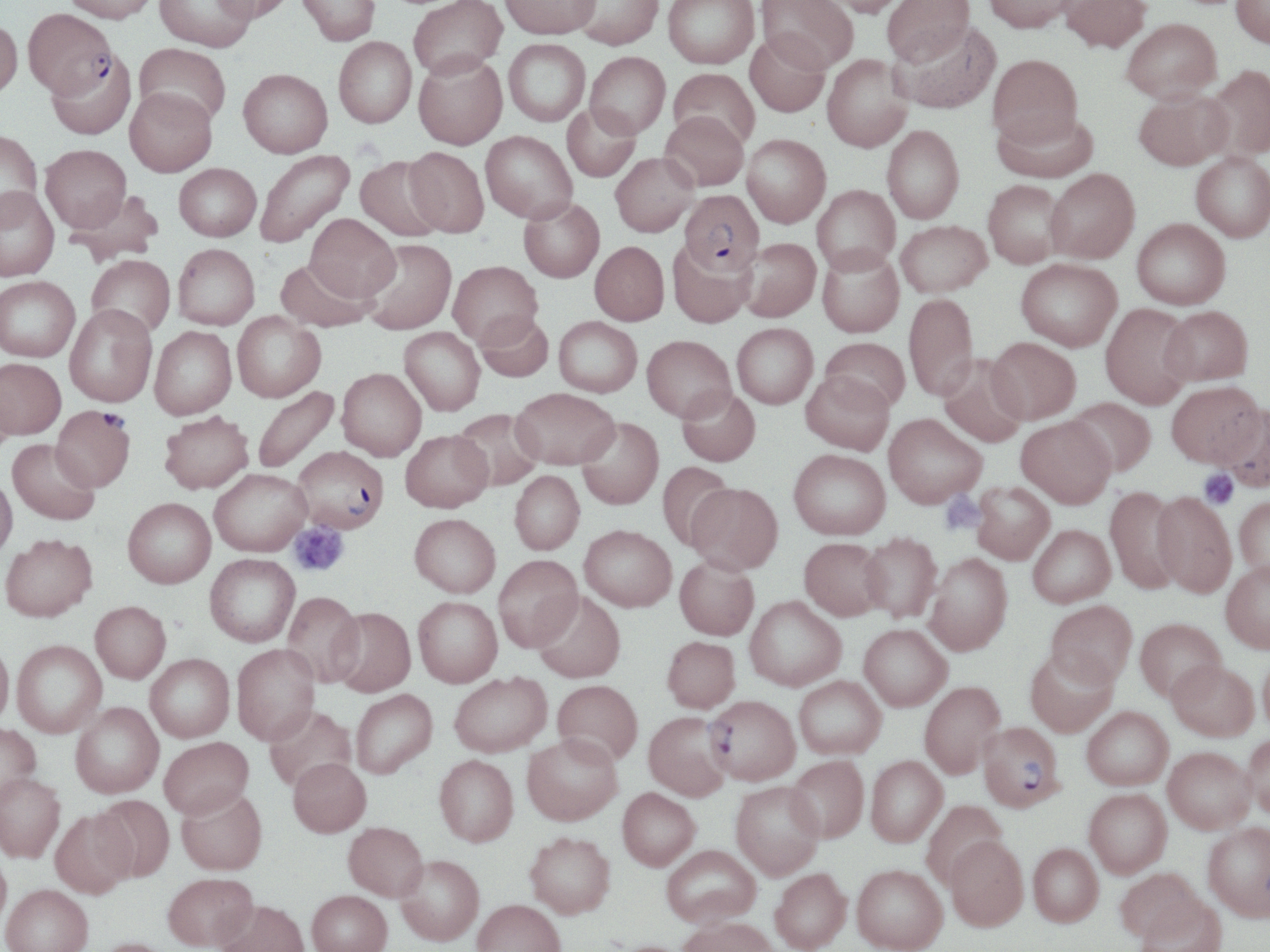
Approximate bounding boxes as (x1,y1)-(x2,y2) corner pairs in pixels. Plasmodium falciparum-infected red blood cell locations: (24,9)-(115,102), (679,190)-(764,275), (51,406)-(135,492), (293,445)-(389,533), (705,695)-(800,785), (978,721)-(1064,811). Uninfected red blood cell locations: (62,0)-(158,26), (154,0)-(258,53), (210,0)-(294,26), (296,0)-(380,46), (409,0)-(507,82), (500,0)-(600,39), (570,0)-(664,51), (663,0)-(759,70), (756,0)-(857,73), (820,0)-(908,18), (883,0)-(975,68), (984,0)-(1079,34), (1059,0)-(1151,55), (1232,0)-(1270,49), (0,19)-(23,102), (1121,20)-(1221,105), (892,21)-(1001,114), (745,33)-(831,118), (333,38)-(417,130), (503,39)-(590,127), (134,44)-(230,128), (585,52)-(670,139), (47,53)-(136,141), (822,54)-(913,152), (988,54)-(1084,148), (413,55)-(507,151), (1205,65)-(1270,161), (668,68)-(759,151), (238,70)-(332,160), (125,90)-(217,178), (1134,90)-(1233,170), (562,104)-(641,182), (993,108)-(1098,183), (660,111)-(749,191), (882,125)-(964,223), (481,130)-(577,223), (0,131)-(43,224), (742,134)-(831,227), (40,146)-(131,233), (404,147)-(489,238), (255,150)-(354,249), (611,152)-(700,237), (1191,152)-(1270,242), (355,156)-(446,243), (174,163)-(262,242), (1045,168)-(1139,263), (983,179)-(1067,268), (812,185)-(900,274), (0,188)-(59,282), (66,189)-(163,267), (518,198)-(605,282), (305,214)-(400,301), (1132,218)-(1231,309), (896,220)-(992,297), (736,237)-(821,322), (358,238)-(457,335), (667,239)-(756,327), (590,241)-(669,325), (173,243)-(260,330), (817,246)-(904,338), (87,255)-(175,339), (275,257)-(377,332), (1016,258)-(1122,350), (448,260)-(542,348), (0,276)-(80,362), (903,293)-(978,399), (1100,303)-(1195,408), (64,305)-(157,407), (1161,305)-(1253,385), (474,310)-(554,382), (232,312)-(326,402), (554,316)-(642,397), (732,323)-(818,408), (149,326)-(237,419), (398,327)-(485,415), (642,335)-(735,422), (987,336)-(1080,423), (819,337)-(910,413), (938,354)-(1028,448), (0,357)-(66,439), (337,368)-(427,461), (800,370)-(894,455), (1,379)-(16,464), (1167,380)-(1265,467), (252,385)-(340,474), (677,386)-(761,466), (511,387)-(620,469), (1066,397)-(1156,476), (1221,402)-(1270,492), (452,407)-(545,491), (159,410)-(254,494), (883,413)-(986,508), (1016,416)-(1116,507), (576,417)-(664,509), (400,429)-(493,512), (8,439)-(100,525), (788,448)-(890,539), (657,461)-(736,550), (209,468)-(310,556), (510,470)-(584,555), (0,474)-(17,560), (972,481)-(1055,564), (686,482)-(783,575), (1105,486)-(1185,593), (1151,492)-(1236,596), (1235,495)-(1270,582), (123,498)-(216,588), (409,513)-(501,597), (580,524)-(677,611), (1028,524)-(1115,607), (860,531)-(942,622), (1,533)-(97,621), (799,536)-(887,620), (924,552)-(1012,655), (204,553)-(300,646), (493,555)-(583,651), (674,555)-(759,640), (1220,559)-(1270,653), (532,590)-(626,683), (282,592)-(365,687), (745,595)-(846,691), (413,596)-(502,687), (1046,600)-(1137,687), (90,601)-(171,683), (329,607)-(416,697), (1136,617)-(1226,701), (859,624)-(952,711), (662,636)-(740,712), (12,640)-(107,737), (0,641)-(14,728), (232,645)-(320,744), (1259,645)-(1270,738), (1025,649)-(1117,737), (145,653)-(234,742), (1168,660)-(1259,740), (449,672)-(552,756), (794,675)-(886,759), (552,679)-(643,766), (919,681)-(1005,778), (350,689)-(437,779), (71,702)-(164,798), (264,705)-(357,792), (1082,707)-(1173,790), (644,711)-(732,801), (0,723)-(40,805), (1243,732)-(1270,819), (522,734)-(622,824), (159,736)-(253,818), (1163,746)-(1255,833), (434,755)-(518,846), (787,755)-(869,842), (866,755)-(947,846), (288,757)-(371,837), (0,772)-(65,862), (731,781)-(824,879), (176,787)-(267,875), (618,787)-(700,870), (1084,788)-(1172,877), (92,794)-(175,881), (921,799)-(1007,888), (50,808)-(135,899), (343,821)-(428,901), (1203,823)-(1270,920), (525,831)-(616,918), (944,835)-(1028,930), (1029,843)-(1103,926), (661,844)-(760,928), (0,849)-(12,932), (395,854)-(484,945), (851,864)-(948,952), (770,868)-(851,952), (1115,868)-(1207,945), (163,872)-(257,950), (1,884)-(93,952), (307,890)-(392,952), (1134,893)-(1227,952), (472,898)-(565,952), (215,899)-(309,952), (676,916)-(782,952), (92,937)-(177,952). Platelet locations: (1199,469)-(1238,509), (940,493)-(985,535), (289,522)-(349,577). Slide-level diagnosis: Plasmodium falciparum. May-Grünwald-Giemsa-stained preparation. Thin blood smear. Light microscopy. Single field of view. Image is 1270×952 pixels. 1000x magnification.